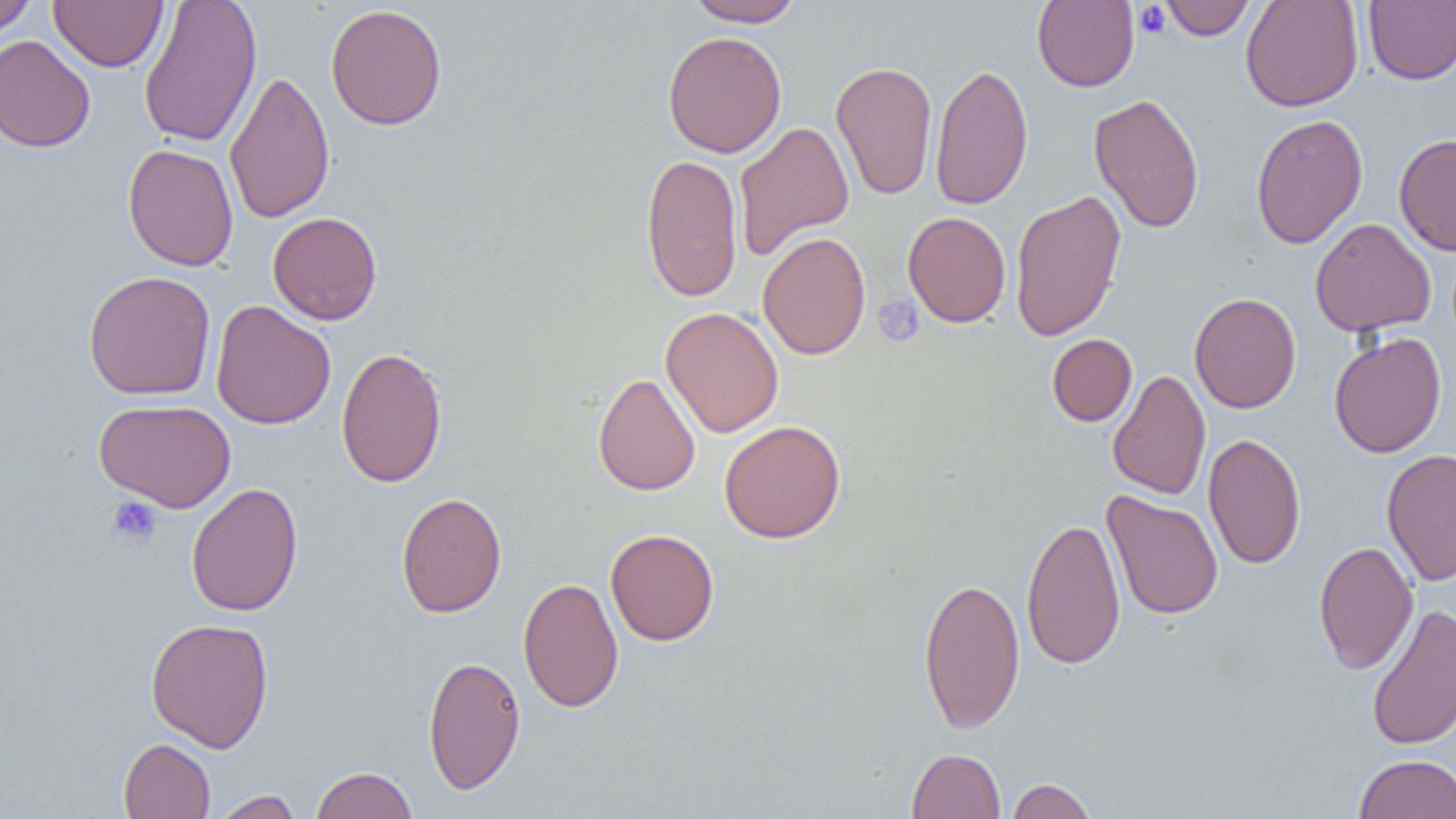

Approximate bounding boxes as (x1,y1)-(x2,y2) corner pairs in pixels. Platelet locations: (1133,3)-(1171,40), (873,294)-(924,346), (107,496)-(163,547). Uninfected red blood cell locations: (0,0)-(36,35), (138,0)-(262,149), (685,0)-(805,27), (1032,0)-(1139,92), (1159,0)-(1256,40), (1240,0)-(1364,112), (1363,0)-(1456,85), (49,1)-(167,71), (325,3)-(447,131), (662,31)-(787,158), (0,35)-(95,152), (830,60)-(937,200), (930,62)-(1033,210), (224,69)-(335,224), (1088,92)-(1205,234), (1250,113)-(1368,249), (733,120)-(854,261), (1394,133)-(1456,257), (122,144)-(239,271), (641,153)-(742,302), (1009,188)-(1127,343), (268,211)-(382,325), (902,211)-(1011,327), (1310,218)-(1436,337), (757,231)-(871,360), (83,270)-(216,400), (1189,292)-(1301,414), (211,300)-(336,430), (660,306)-(784,438), (1329,332)-(1447,458), (1047,334)-(1137,426), (336,345)-(448,488), (1107,369)-(1210,500), (593,372)-(700,495), (94,398)-(236,512), (718,420)-(847,544), (1203,432)-(1306,569), (1381,448)-(1456,586), (186,482)-(303,616), (1102,490)-(1223,621), (396,492)-(507,618), (1021,515)-(1126,670), (606,528)-(719,646), (1313,541)-(1418,674), (918,575)-(1025,734), (518,576)-(623,712), (1365,603)-(1456,752), (145,617)-(274,752), (422,654)-(526,795), (118,738)-(215,818), (906,747)-(1006,819), (1354,754)-(1456,818), (310,766)-(417,818), (1005,777)-(1097,818), (211,790)-(305,818). Slide-level diagnosis: no evidence of blood parasites. Light microscopy. Image is 1456×819 pixels. One field of a larger specimen. 1000x magnification. Thin blood smear.